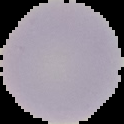
Summary:
  - Result: no Plasmodium parasites detected
  - Image type: segmented cell region on a black background
  - Image size: 124×124 pixels
  - Preparation: thin blood film